State the blood parasite species.
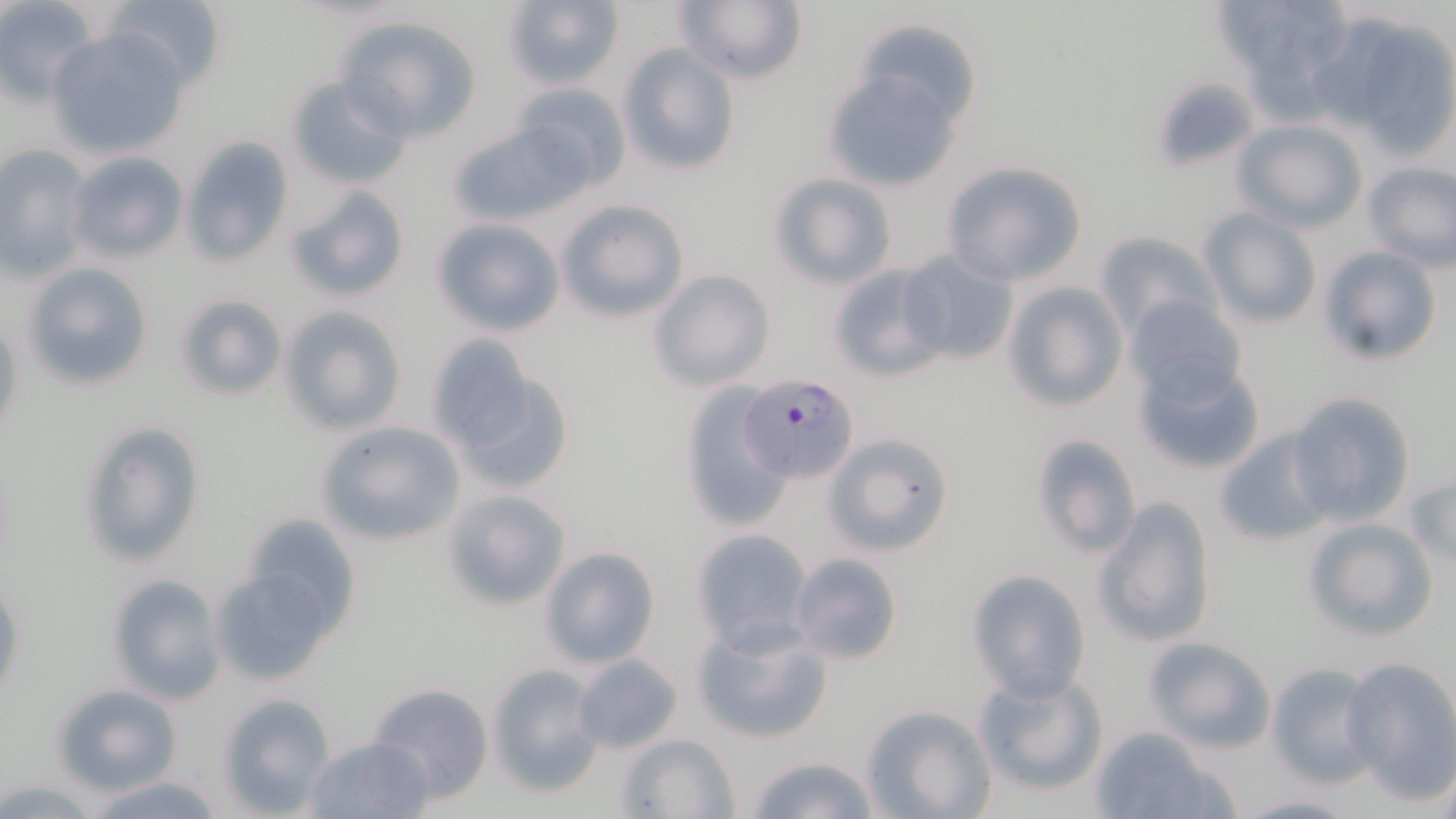
Plasmodium falciparum.

Summary:
  - Coordinate format: approximate bounding boxes as [x1, y1, x2, y2] in pixels
  - Plasmodium falciparum-infected red blood cell locations: [738, 374, 861, 482]
  - Uninfected red blood cell locations: [106, 0, 226, 93], [503, 0, 624, 90], [675, 0, 809, 86], [1216, 0, 1354, 107], [0, 4, 95, 106], [1320, 10, 1456, 155], [332, 13, 485, 142], [47, 26, 191, 161], [617, 43, 740, 177], [821, 63, 968, 193], [286, 73, 413, 190], [508, 81, 631, 193], [444, 116, 593, 228], [1231, 121, 1366, 232], [181, 135, 293, 267], [0, 146, 91, 282], [66, 151, 188, 264], [940, 160, 1088, 285], [1361, 161, 1455, 272], [767, 171, 899, 289], [285, 183, 409, 305], [556, 199, 690, 322], [1202, 209, 1323, 330], [430, 216, 565, 336], [1093, 230, 1221, 340], [1316, 245, 1444, 367], [898, 246, 1020, 366], [22, 261, 153, 391], [828, 263, 951, 382], [649, 269, 775, 391], [1000, 281, 1127, 413], [175, 292, 289, 401], [1124, 296, 1248, 403], [280, 306, 407, 434], [0, 317, 24, 447], [424, 331, 547, 464], [1131, 350, 1266, 476], [444, 366, 574, 496], [677, 380, 795, 532], [1287, 391, 1417, 527], [75, 419, 207, 569], [316, 420, 466, 546], [1212, 426, 1336, 547], [825, 431, 953, 557], [1027, 431, 1143, 560], [1406, 472, 1455, 568], [440, 487, 572, 612], [1093, 497, 1219, 648], [232, 511, 365, 639], [1303, 517, 1438, 643], [689, 527, 815, 651], [540, 546, 661, 670], [790, 552, 905, 666], [209, 558, 349, 687], [967, 569, 1091, 699], [106, 571, 226, 704], [0, 578, 26, 708], [691, 615, 835, 746], [1142, 635, 1278, 753], [572, 654, 684, 753], [1340, 655, 1456, 800], [1265, 662, 1381, 788], [486, 663, 607, 798], [971, 668, 1109, 797], [52, 683, 183, 796], [365, 683, 494, 804], [217, 692, 335, 815], [862, 704, 995, 819], [1088, 724, 1232, 819], [617, 732, 739, 817], [303, 734, 437, 818], [745, 753, 883, 819], [84, 773, 228, 819], [1235, 793, 1362, 817]
  - Modality: light microscopy
  - Field of view: one of a larger specimen
  - Preparation: thin blood smear
  - Image size: 1456×819 pixels
  - Stain: May-Grünwald-Giemsa
  - Magnification: 1000x